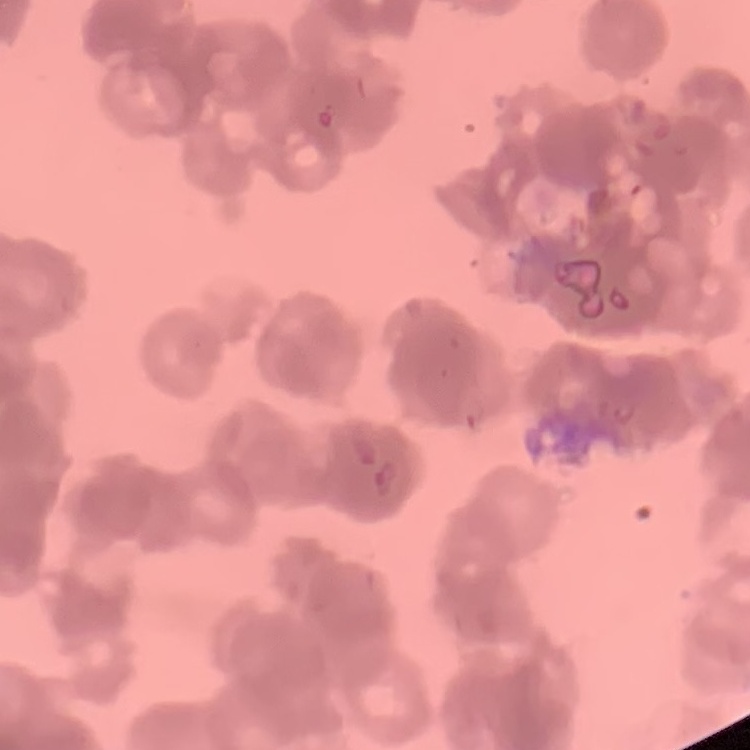

Summary:
  - Erythrocyte morphology: rouleaux formation
  - Preparation: thin blood film
  - Image type: one tile cut from a larger photomicrograph
  - Stain: Field's or Giemsa